Locate and identify every blood parasite.
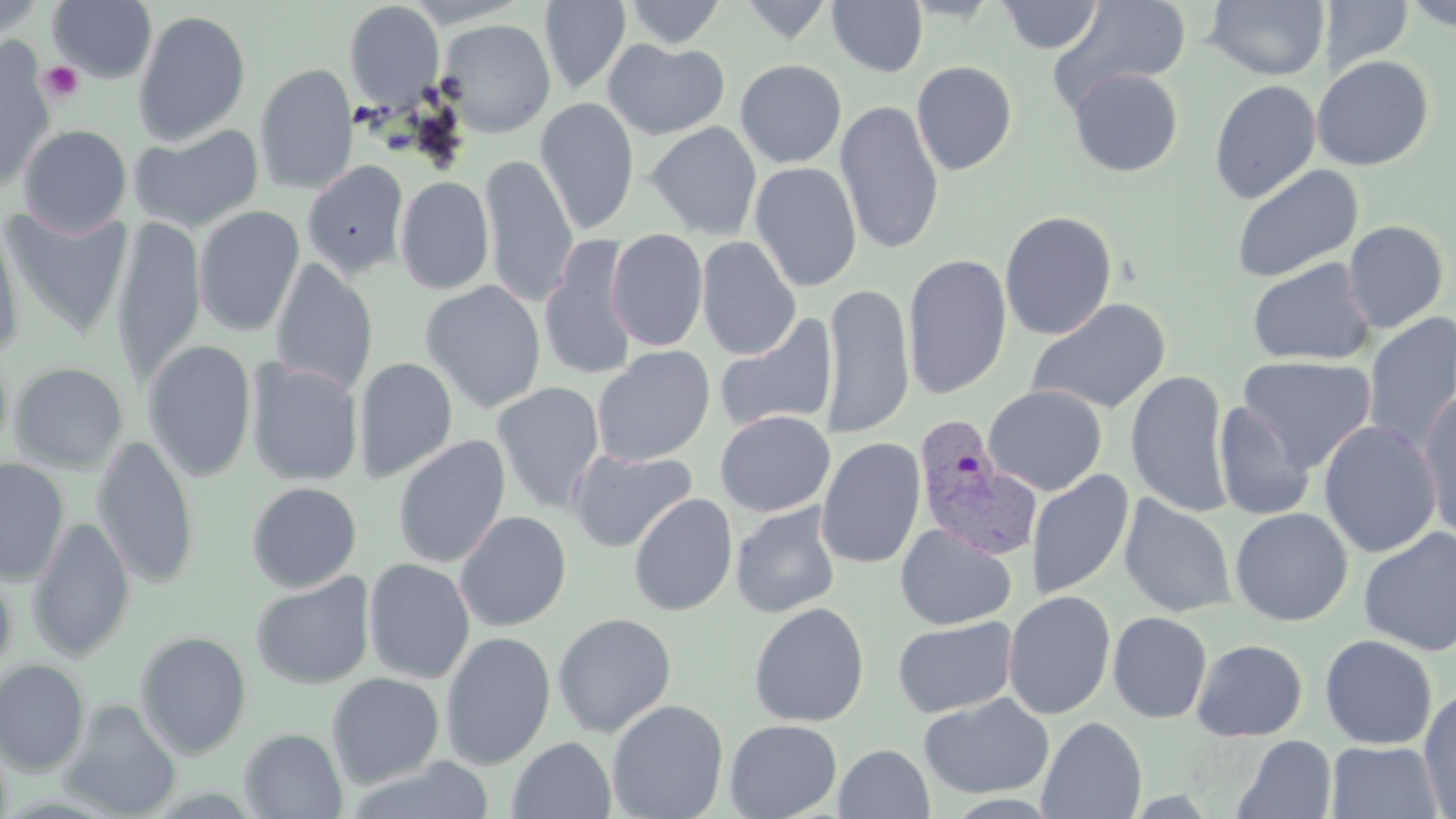
Approximate bounding boxes as named x1/y1/x2/y2 corners in pixels.
Plasmodium vivax-infected red blood cells: (x1=912, y1=418, x2=1040, y2=559).
No Plasmodium falciparum, Plasmodium ovale, Plasmodium malariae, Babesia divergens, or Trypanosoma brucei observed.

slide-level diagnosis = Plasmodium vivax
preparation = thin blood film
magnification = 1000x
image size = 1456×819 pixels
uninfected red blood cell locations = approximate bounding boxes as named x1/y1/x2/y2 corners in pixels: (x1=47, y1=0, x2=158, y2=83), (x1=623, y1=0, x2=727, y2=49), (x1=739, y1=0, x2=835, y2=43), (x1=1047, y1=0, x2=1192, y2=109), (x1=1204, y1=0, x2=1330, y2=81), (x1=1322, y1=0, x2=1413, y2=78), (x1=1402, y1=0, x2=1456, y2=32), (x1=344, y1=1, x2=446, y2=110), (x1=540, y1=1, x2=631, y2=95), (x1=827, y1=1, x2=928, y2=77), (x1=995, y1=1, x2=1103, y2=54), (x1=0, y1=3, x2=44, y2=44), (x1=133, y1=9, x2=251, y2=146), (x1=435, y1=18, x2=556, y2=137), (x1=603, y1=39, x2=730, y2=140), (x1=0, y1=44, x2=55, y2=191), (x1=1311, y1=55, x2=1434, y2=171), (x1=735, y1=59, x2=846, y2=168), (x1=911, y1=61, x2=1017, y2=176), (x1=254, y1=63, x2=357, y2=195), (x1=1068, y1=68, x2=1183, y2=177), (x1=1209, y1=79, x2=1321, y2=204), (x1=535, y1=97, x2=640, y2=235), (x1=835, y1=100, x2=945, y2=255), (x1=646, y1=121, x2=762, y2=240), (x1=129, y1=123, x2=264, y2=232), (x1=18, y1=124, x2=132, y2=236), (x1=480, y1=155, x2=578, y2=308), (x1=303, y1=160, x2=409, y2=279), (x1=750, y1=161, x2=862, y2=292), (x1=1231, y1=165, x2=1363, y2=282), (x1=395, y1=175, x2=495, y2=295), (x1=1, y1=205, x2=132, y2=339), (x1=194, y1=205, x2=305, y2=337), (x1=999, y1=210, x2=1118, y2=340), (x1=0, y1=213, x2=24, y2=360), (x1=111, y1=216, x2=205, y2=388), (x1=1343, y1=220, x2=1449, y2=333), (x1=606, y1=228, x2=708, y2=352), (x1=540, y1=234, x2=638, y2=382), (x1=696, y1=236, x2=801, y2=359), (x1=903, y1=254, x2=1012, y2=400), (x1=269, y1=258, x2=378, y2=398), (x1=1247, y1=258, x2=1375, y2=366), (x1=420, y1=280, x2=546, y2=413), (x1=821, y1=282, x2=914, y2=438), (x1=1026, y1=297, x2=1171, y2=415), (x1=714, y1=312, x2=837, y2=433), (x1=1362, y1=312, x2=1456, y2=457), (x1=143, y1=339, x2=257, y2=483), (x1=592, y1=345, x2=715, y2=466), (x1=1237, y1=355, x2=1377, y2=473), (x1=354, y1=356, x2=458, y2=483), (x1=244, y1=359, x2=364, y2=486), (x1=9, y1=361, x2=128, y2=474), (x1=1126, y1=370, x2=1233, y2=518), (x1=491, y1=382, x2=605, y2=514), (x1=983, y1=385, x2=1107, y2=496), (x1=1418, y1=391, x2=1456, y2=542), (x1=1214, y1=401, x2=1314, y2=521), (x1=715, y1=410, x2=834, y2=517), (x1=1318, y1=420, x2=1441, y2=558), (x1=93, y1=434, x2=199, y2=590), (x1=392, y1=435, x2=511, y2=569), (x1=816, y1=437, x2=925, y2=570), (x1=567, y1=447, x2=697, y2=552), (x1=0, y1=459, x2=69, y2=585), (x1=1027, y1=470, x2=1134, y2=600), (x1=246, y1=481, x2=362, y2=592), (x1=628, y1=493, x2=738, y2=616), (x1=1119, y1=495, x2=1237, y2=617), (x1=730, y1=502, x2=842, y2=618), (x1=1230, y1=507, x2=1352, y2=626), (x1=454, y1=510, x2=572, y2=631), (x1=28, y1=516, x2=135, y2=662), (x1=896, y1=523, x2=1016, y2=630), (x1=1358, y1=528, x2=1456, y2=656), (x1=363, y1=558, x2=476, y2=684), (x1=0, y1=566, x2=16, y2=676), (x1=251, y1=572, x2=375, y2=689), (x1=1003, y1=590, x2=1117, y2=720), (x1=748, y1=602, x2=870, y2=727), (x1=1107, y1=611, x2=1213, y2=723), (x1=552, y1=612, x2=677, y2=737), (x1=892, y1=616, x2=1017, y2=717), (x1=135, y1=631, x2=252, y2=759), (x1=439, y1=631, x2=556, y2=771), (x1=1319, y1=634, x2=1438, y2=750), (x1=1191, y1=638, x2=1308, y2=742), (x1=0, y1=659, x2=90, y2=776), (x1=326, y1=672, x2=445, y2=788), (x1=1418, y1=689, x2=1456, y2=817), (x1=918, y1=693, x2=1053, y2=799), (x1=59, y1=698, x2=182, y2=818), (x1=607, y1=699, x2=729, y2=819), (x1=1037, y1=716, x2=1147, y2=819), (x1=724, y1=719, x2=842, y2=819), (x1=240, y1=728, x2=347, y2=818), (x1=1231, y1=735, x2=1337, y2=819), (x1=507, y1=737, x2=617, y2=819), (x1=1325, y1=740, x2=1444, y2=818), (x1=834, y1=744, x2=934, y2=818), (x1=345, y1=758, x2=497, y2=818)
platelet locations = approximate bounding boxes as named x1/y1/x2/y2 corners in pixels: (x1=38, y1=60, x2=84, y2=104)
field of view = one of a larger specimen
modality = light microscopy
stain = May-Grünwald-Giemsa